Give the preparation type.
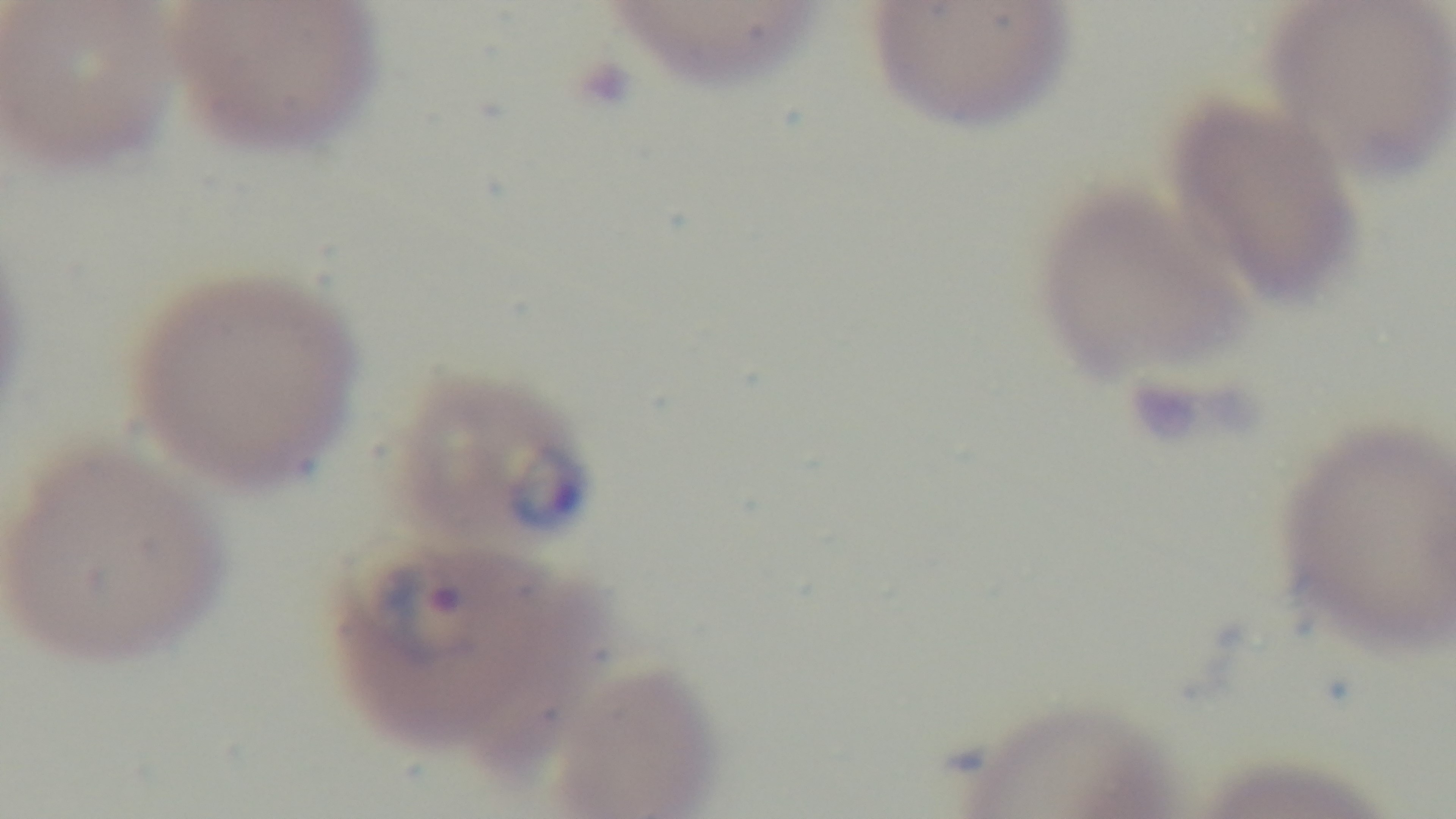

A thin smear.

Summary:
  - Modality: light microscopy
  - Capture: mounted 4K digital camera
  - Field of view: single
  - Malaria status: positive
  - Objective: 100x oil immersion
  - Stain: Giemsa